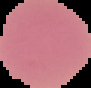 Image is 91×88 pixels. From a thin blood film. Malaria status: uninfected. The area outside the segmented cell region is set to black.